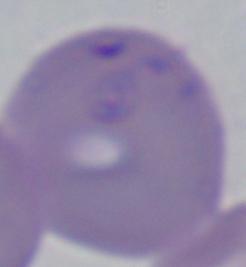
Summary:
  - Identification: Babesia
  - Modality: photomicrograph
  - Magnification: 1000x